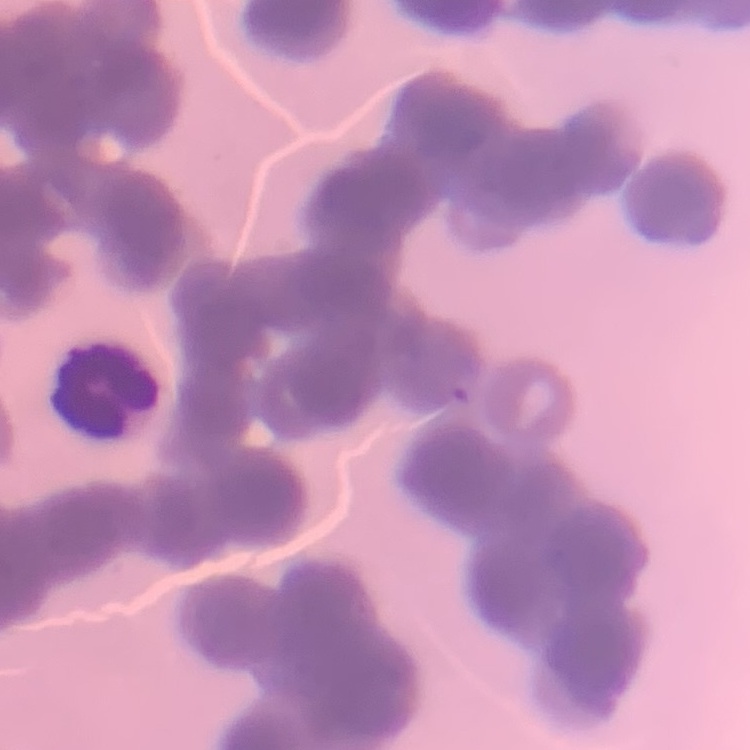

The erythrocytes exhibit rouleaux formation. Field's or Giemsa stain. One tile cut from a larger photomicrograph. Thin blood film.